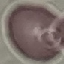
malaria status = uninfected
capture = smartphone camera at the microscope eyepiece
stain = Giemsa
preparation = thin blood smear
image type = automatically extracted cell patch, resized to 64 × 64 pixels